Assess this cell for malaria.
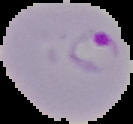
Parasitized.

Summary:
  - Preparation: thin blood film
  - Image size: 133×124 pixels
  - Image type: segmented cell region with the area outside set to black